Comment on the morphology of the erythrocytes.
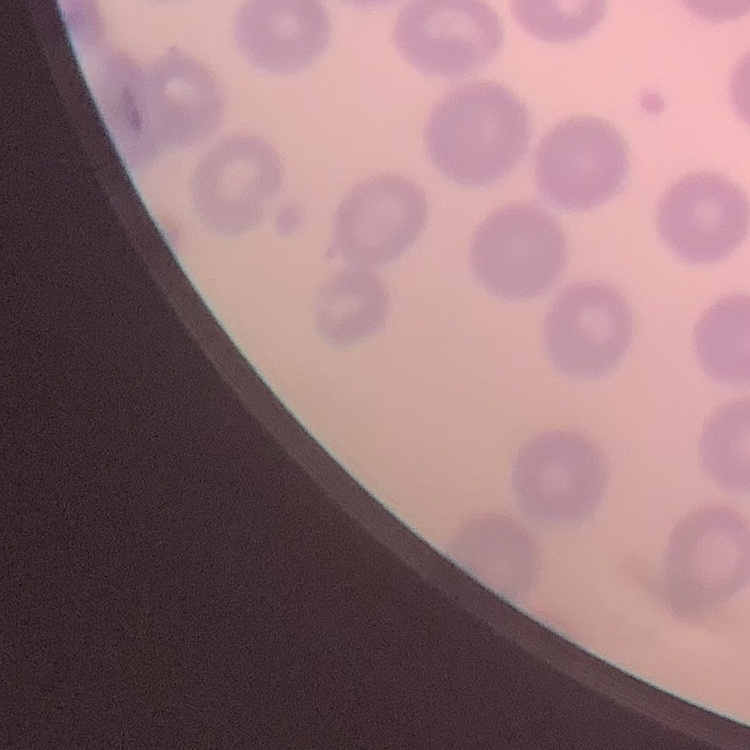

No rouleaux formation.

preparation: thin peripheral smear
image_type: one tile cut from a larger photomicrograph
stain: Field's or Giemsa